Comment on the morphology of the red blood cells.
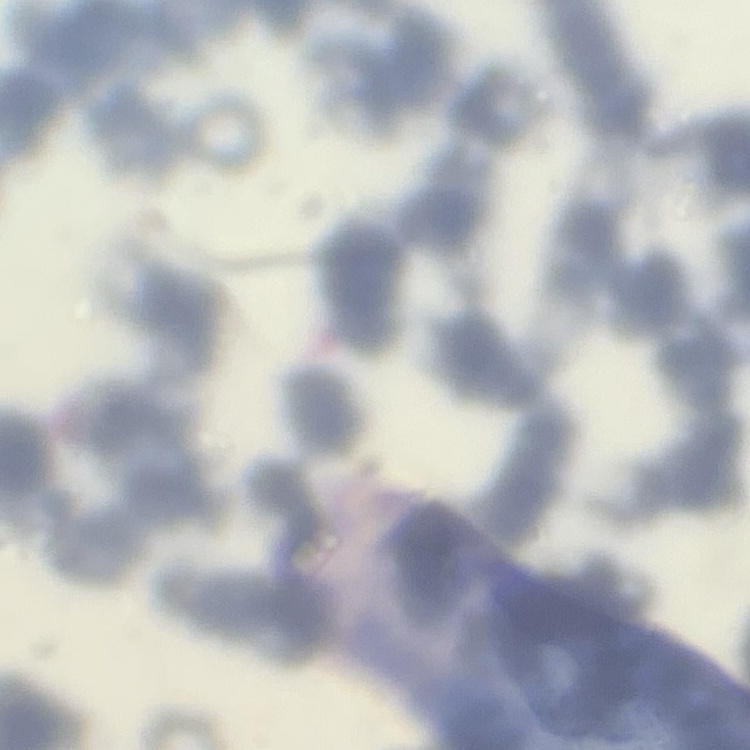
They show rouleaux formation.

stain = Field's or Giemsa
preparation = thin peripheral smear
image type = square crop of a larger photomicrograph